Outline each Plasmodium falciparum-infected red blood cell.
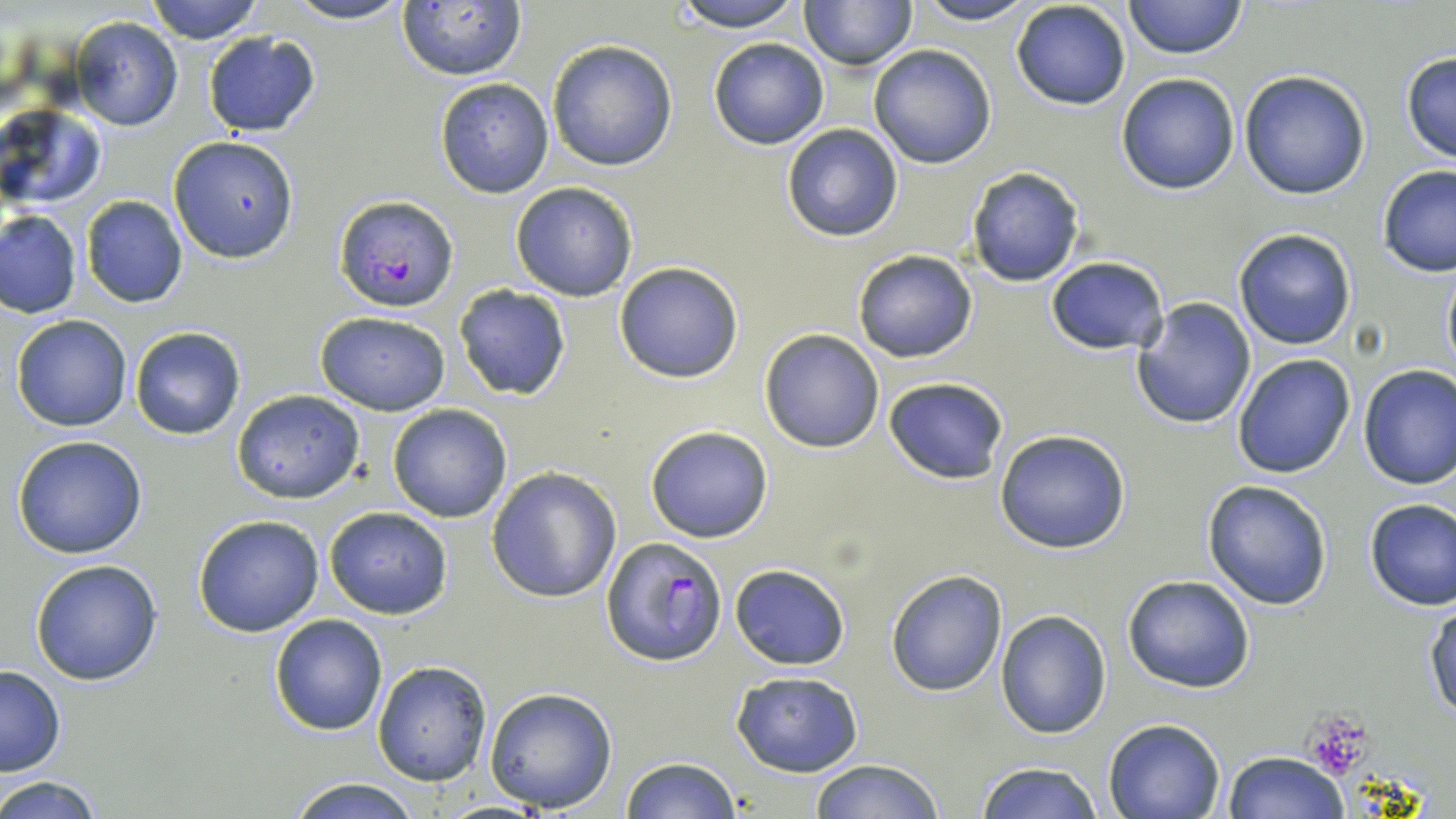
Approximate bounding boxes as named x1/y1/x2/y2 corners in pixels.
Plasmodium falciparum-infected red blood cells: (x1=335, y1=196, x2=459, y2=313), (x1=600, y1=536, x2=726, y2=667).

slide-level diagnosis = Plasmodium falciparum
magnification = 1000x
image size = 1456×819 pixels
uninfected red blood cell locations = approximate bounding boxes as named x1/y1/x2/y2 corners in pixels: (x1=146, y1=0, x2=266, y2=43), (x1=282, y1=0, x2=417, y2=25), (x1=668, y1=0, x2=809, y2=32), (x1=799, y1=0, x2=916, y2=70), (x1=911, y1=0, x2=1040, y2=25), (x1=1124, y1=0, x2=1248, y2=59), (x1=1009, y1=1, x2=1131, y2=110), (x1=397, y1=2, x2=528, y2=80), (x1=68, y1=17, x2=185, y2=131), (x1=201, y1=31, x2=322, y2=137), (x1=708, y1=38, x2=829, y2=150), (x1=547, y1=40, x2=678, y2=171), (x1=869, y1=44, x2=997, y2=169), (x1=1399, y1=50, x2=1456, y2=164), (x1=1240, y1=71, x2=1370, y2=198), (x1=1116, y1=73, x2=1239, y2=193), (x1=435, y1=78, x2=553, y2=198), (x1=1, y1=104, x2=106, y2=209), (x1=782, y1=123, x2=904, y2=242), (x1=167, y1=135, x2=299, y2=264), (x1=1377, y1=165, x2=1456, y2=277), (x1=966, y1=167, x2=1085, y2=286), (x1=511, y1=182, x2=638, y2=301), (x1=81, y1=195, x2=188, y2=309), (x1=1, y1=209, x2=82, y2=318), (x1=1233, y1=228, x2=1358, y2=351), (x1=852, y1=249, x2=979, y2=364), (x1=1046, y1=256, x2=1169, y2=355), (x1=613, y1=261, x2=744, y2=384), (x1=1441, y1=261, x2=1455, y2=376), (x1=453, y1=284, x2=572, y2=402), (x1=1131, y1=297, x2=1256, y2=430), (x1=316, y1=313, x2=451, y2=416), (x1=11, y1=314, x2=133, y2=431), (x1=130, y1=326, x2=246, y2=440), (x1=759, y1=328, x2=886, y2=454), (x1=1232, y1=353, x2=1358, y2=478), (x1=1357, y1=365, x2=1456, y2=490), (x1=883, y1=377, x2=1008, y2=486), (x1=232, y1=388, x2=366, y2=504), (x1=387, y1=404, x2=512, y2=522), (x1=644, y1=424, x2=773, y2=542), (x1=994, y1=428, x2=1132, y2=553), (x1=11, y1=435, x2=149, y2=558), (x1=486, y1=466, x2=621, y2=601), (x1=1202, y1=479, x2=1333, y2=611), (x1=1363, y1=498, x2=1456, y2=611), (x1=323, y1=506, x2=453, y2=619), (x1=192, y1=514, x2=324, y2=638), (x1=30, y1=559, x2=164, y2=684), (x1=729, y1=563, x2=850, y2=670), (x1=885, y1=568, x2=1008, y2=696), (x1=1122, y1=574, x2=1256, y2=694), (x1=1425, y1=604, x2=1456, y2=724), (x1=994, y1=608, x2=1110, y2=739), (x1=269, y1=613, x2=388, y2=735), (x1=372, y1=660, x2=493, y2=785), (x1=0, y1=666, x2=66, y2=777), (x1=730, y1=669, x2=864, y2=776), (x1=484, y1=686, x2=619, y2=813), (x1=1102, y1=717, x2=1226, y2=819), (x1=1223, y1=751, x2=1349, y2=818), (x1=619, y1=757, x2=743, y2=818), (x1=808, y1=758, x2=946, y2=818), (x1=973, y1=761, x2=1104, y2=819), (x1=2, y1=776, x2=106, y2=818), (x1=281, y1=777, x2=426, y2=818)
modality = light microscopy
preparation = thin blood film
field of view = single
stain = May-Grünwald-Giemsa
platelet locations = approximate bounding boxes as named x1/y1/x2/y2 corners in pixels: (x1=1303, y1=716, x2=1370, y2=777)